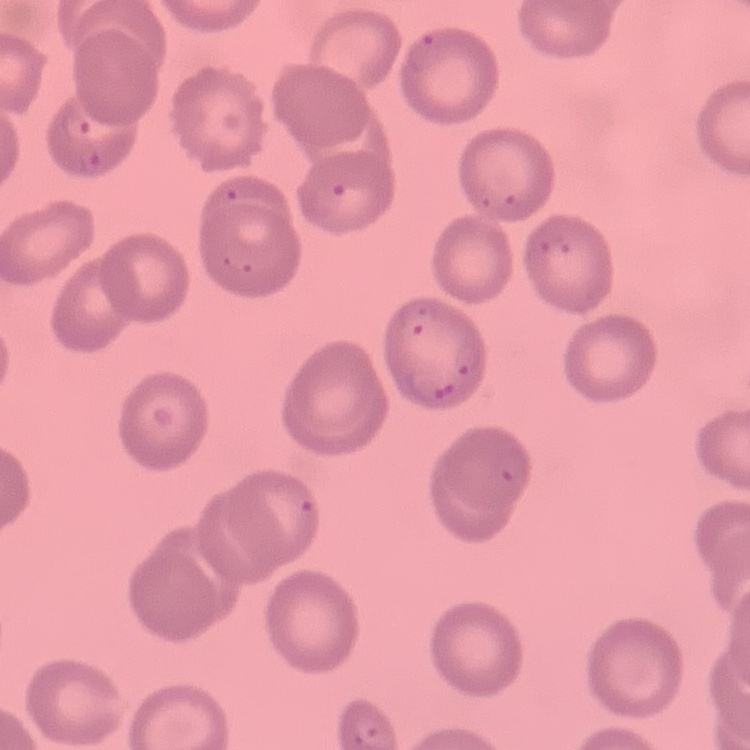

red_blood_cell_morphology: no rouleaux formation
stain: Field's or Giemsa
preparation: thin peripheral smear
image_type: one tile cut from a larger photomicrograph